Classify this cell by malaria status.
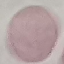
Uninfected.

capture = smartphone camera at the microscope eyepiece
image type = automatically extracted cell patch, resized to 64 × 64 pixels
stain = Giemsa
preparation = thin blood smear